Outline each Plasmodium vivax-infected red blood cell.
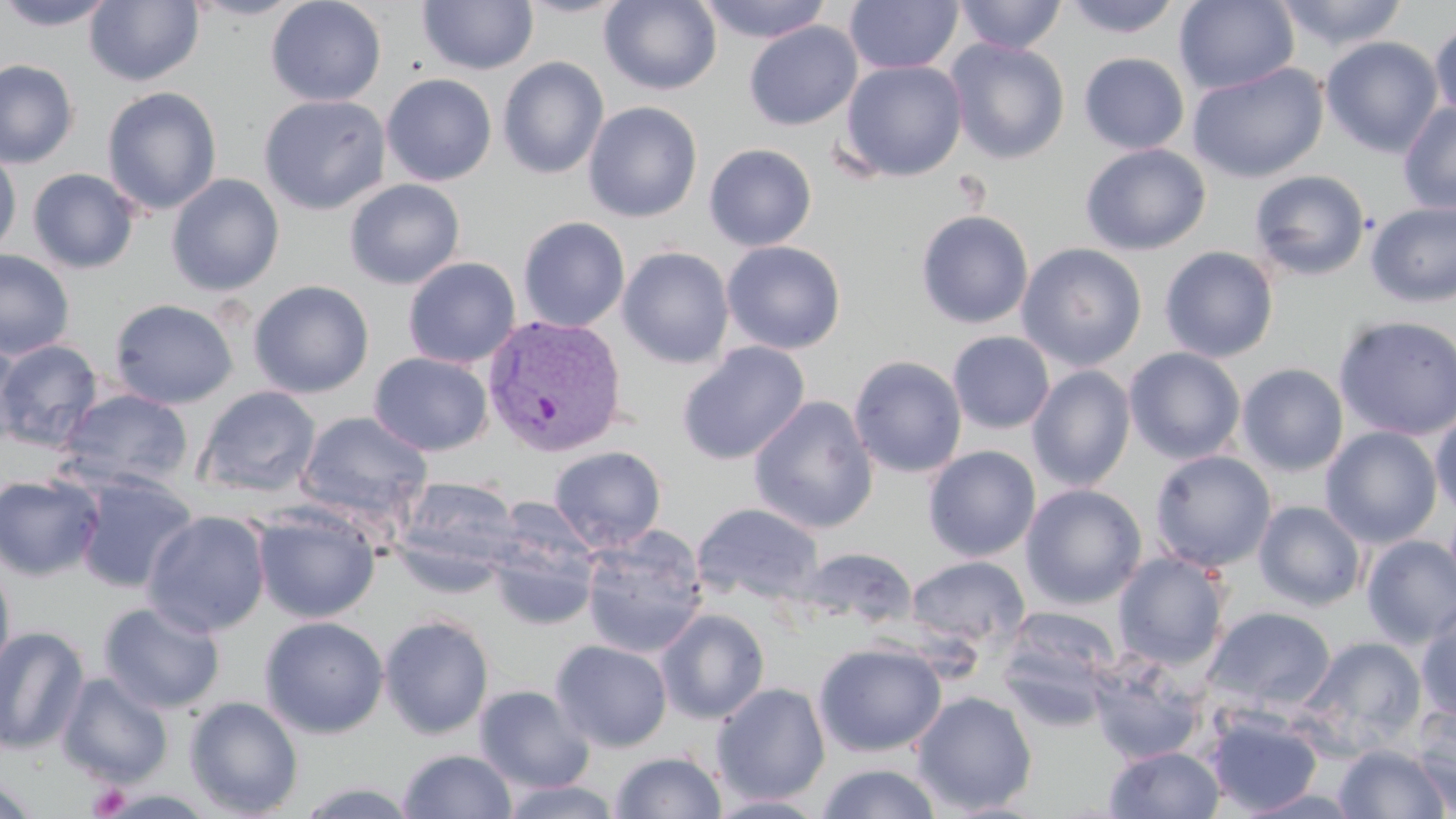

Approximate bounding boxes as (x1, y1, x2, y2) in pixels.
Plasmodium vivax-infected red blood cells: (482, 315, 627, 457).

{
  "slide_level_diagnosis": "Plasmodium vivax",
  "platelet_locations": "approximate bounding boxes as (x1, y1, x2, y2) in pixels: (88, 783, 132, 818)",
  "uninfected_red_blood_cell_locations": "approximate bounding boxes as (x1, y1, x2, y2) in pixels: (0, 0, 117, 31), (85, 0, 204, 86), (183, 0, 308, 21), (266, 0, 387, 107), (514, 0, 633, 19), (599, 0, 722, 95), (696, 0, 833, 43), (844, 0, 963, 74), (954, 0, 1067, 55), (1061, 0, 1185, 38), (1175, 0, 1299, 95), (1273, 0, 1408, 52), (417, 1, 539, 75), (1429, 19, 1456, 123), (743, 21, 862, 130), (1320, 36, 1444, 158), (946, 39, 1070, 164), (1078, 52, 1190, 155), (497, 57, 609, 179), (0, 59, 80, 169), (839, 59, 969, 182), (1188, 63, 1328, 183), (382, 73, 497, 186), (101, 86, 222, 216), (258, 94, 391, 215), (583, 101, 703, 223), (1398, 101, 1456, 214), (704, 143, 817, 251), (1080, 143, 1211, 255), (0, 147, 22, 259), (27, 168, 140, 274), (1249, 169, 1371, 281), (166, 174, 285, 297), (344, 179, 466, 290), (1365, 201, 1456, 308), (915, 210, 1034, 329), (518, 216, 630, 332), (722, 241, 846, 355), (1016, 243, 1147, 371), (617, 246, 735, 369), (1159, 246, 1279, 363), (0, 250, 75, 360), (402, 257, 521, 368), (248, 280, 374, 398), (109, 298, 238, 409), (1333, 314, 1456, 441), (948, 331, 1055, 434), (0, 338, 25, 450), (0, 339, 104, 451), (677, 341, 811, 465), (1124, 347, 1246, 464), (369, 352, 493, 456), (848, 355, 967, 478), (1237, 363, 1349, 476), (1027, 366, 1136, 491), (193, 386, 321, 498), (57, 388, 193, 492), (749, 396, 878, 535), (1430, 407, 1456, 521), (295, 411, 433, 526), (1320, 426, 1443, 548), (548, 445, 667, 552), (923, 446, 1041, 562), (1149, 449, 1277, 573), (73, 473, 198, 594), (0, 474, 105, 582), (393, 475, 522, 585), (1020, 483, 1147, 609), (1253, 500, 1367, 611), (692, 503, 824, 605), (253, 504, 381, 623), (142, 510, 272, 637), (486, 516, 600, 632), (581, 526, 709, 658), (1361, 535, 1456, 648), (792, 548, 918, 631), (1113, 552, 1231, 671), (906, 556, 1030, 651), (0, 562, 16, 683), (98, 601, 226, 714), (1416, 604, 1456, 723), (996, 606, 1122, 726), (1202, 606, 1337, 716), (656, 608, 770, 724), (378, 614, 495, 740), (259, 616, 389, 739), (0, 625, 90, 755), (1295, 636, 1428, 756), (550, 640, 673, 752), (813, 642, 947, 757), (1086, 649, 1209, 765), (56, 672, 174, 788), (54, 678, 301, 795), (711, 682, 830, 805), (474, 684, 595, 793), (911, 691, 1038, 815), (184, 696, 304, 818), (1408, 704, 1456, 816), (1203, 708, 1324, 816), (1332, 744, 1452, 819), (1104, 746, 1225, 818), (398, 749, 517, 818), (610, 751, 727, 819), (816, 763, 944, 819), (0, 778, 40, 819), (293, 779, 423, 818), (498, 781, 623, 819), (1234, 788, 1368, 818), (706, 794, 832, 817)",
  "modality": "optical microscopy",
  "image_size": "1456×819 pixels",
  "stain": "May-Grünwald-Giemsa",
  "field_of_view": "single",
  "magnification": "1000x",
  "preparation": "thin blood film"
}